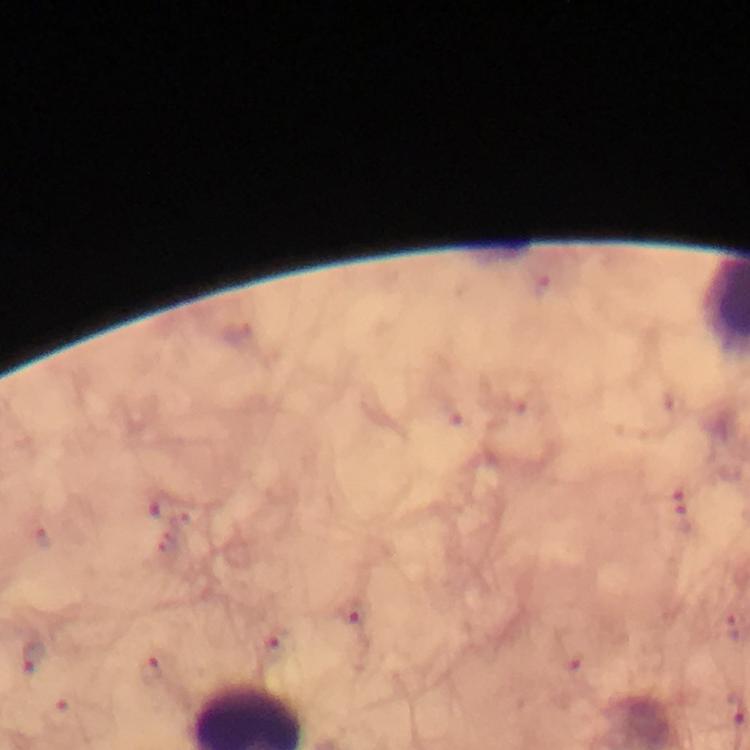
{
  "preparation": "thick smear",
  "stain": "Giemsa",
  "magnification": "100x",
  "malaria_parasite_locations": "approximate object centers, in pixels from the top-left corner: (x=161, y=508), (x=679, y=519), (x=350, y=614), (x=274, y=648), (x=151, y=671)",
  "capture": "smartphone photograph through a microscope",
  "image_size": "750×750 pixels",
  "immersion_oil": "used",
  "context": "from a diagnostic examination for malaria",
  "cropped_from": "one field of view"
}